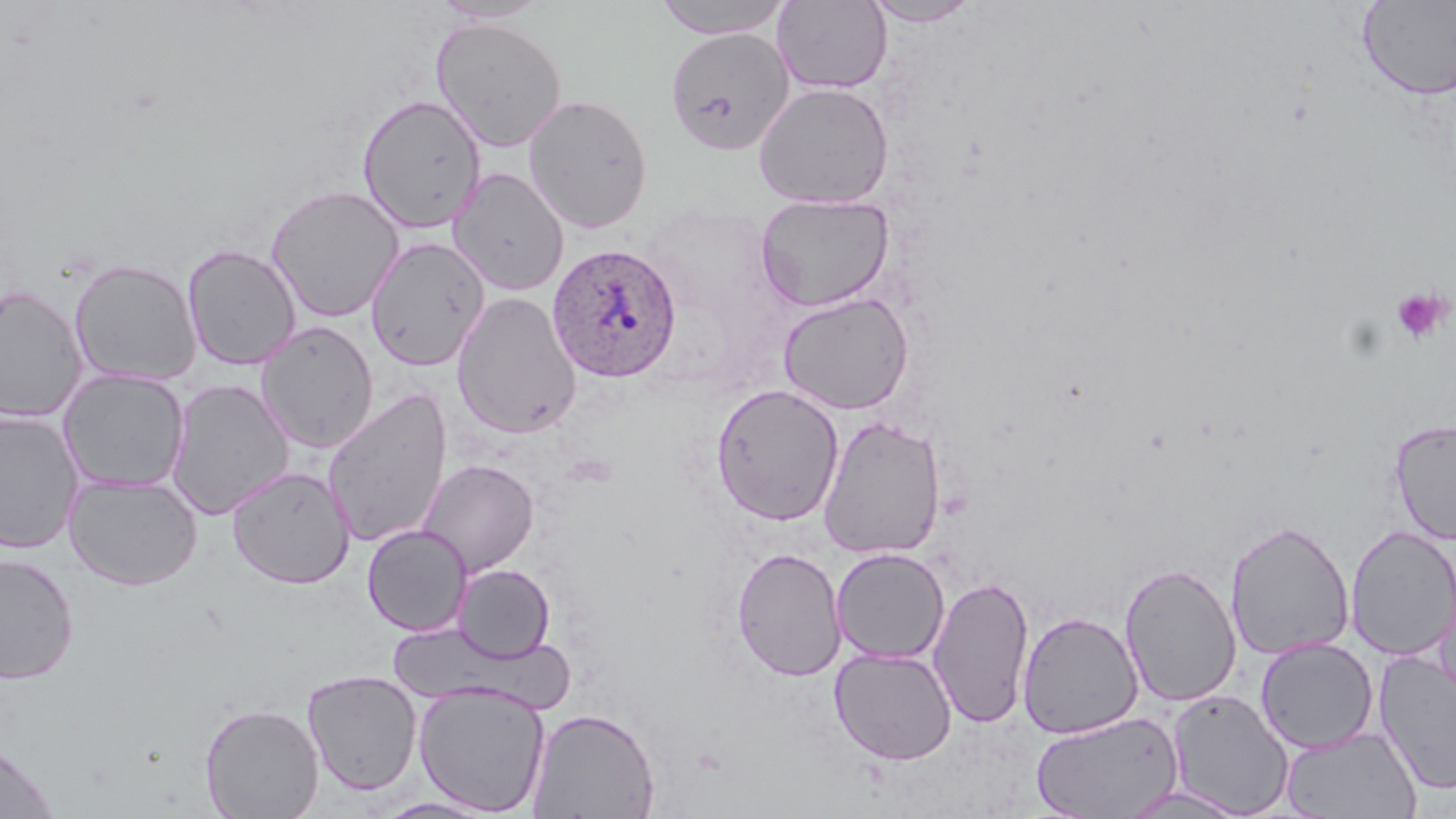

Approximate bounding boxes as (x1, y1, x2, y2) in pixels. Plasmodium ovale-infected red blood cell locations: (546, 243, 683, 383). Platelet locations: (1390, 288, 1453, 346). Uninfected red blood cell locations: (431, 0, 552, 24), (654, 1, 793, 39), (772, 1, 892, 94), (862, 1, 981, 27), (1357, 1, 1456, 101), (431, 16, 568, 152), (665, 26, 794, 155), (753, 81, 894, 209), (356, 93, 487, 233), (522, 93, 653, 234), (449, 166, 570, 296), (266, 184, 405, 322), (755, 192, 894, 312), (365, 236, 491, 372), (182, 243, 301, 370), (69, 258, 202, 387), (0, 285, 89, 424), (451, 291, 582, 439), (778, 291, 915, 415), (255, 320, 379, 454), (58, 368, 191, 494), (165, 377, 295, 520), (710, 383, 845, 526), (322, 386, 453, 548), (0, 409, 84, 555), (817, 414, 946, 560), (1389, 417, 1456, 545), (417, 459, 538, 577), (226, 465, 355, 589), (65, 473, 203, 590), (1225, 519, 1354, 661), (1345, 524, 1456, 661), (362, 525, 472, 636), (731, 546, 847, 682), (831, 547, 950, 665), (0, 552, 79, 685), (1119, 561, 1242, 707), (453, 563, 556, 663), (928, 575, 1034, 729), (1018, 611, 1143, 739), (391, 623, 577, 713), (1255, 637, 1379, 753), (829, 646, 958, 765), (1374, 649, 1456, 795), (301, 669, 422, 797), (413, 681, 550, 816), (1166, 689, 1295, 817), (198, 702, 324, 818), (527, 706, 661, 819), (1031, 711, 1182, 819), (1281, 725, 1421, 818), (0, 739, 59, 819), (1116, 785, 1253, 818), (371, 796, 499, 818). Slide-level diagnosis: Plasmodium ovale. Thin blood film. 1000x magnification. Image is 1456×819 pixels. May-Grünwald-Giemsa-stained preparation. Light microscopy. One field of a larger specimen.